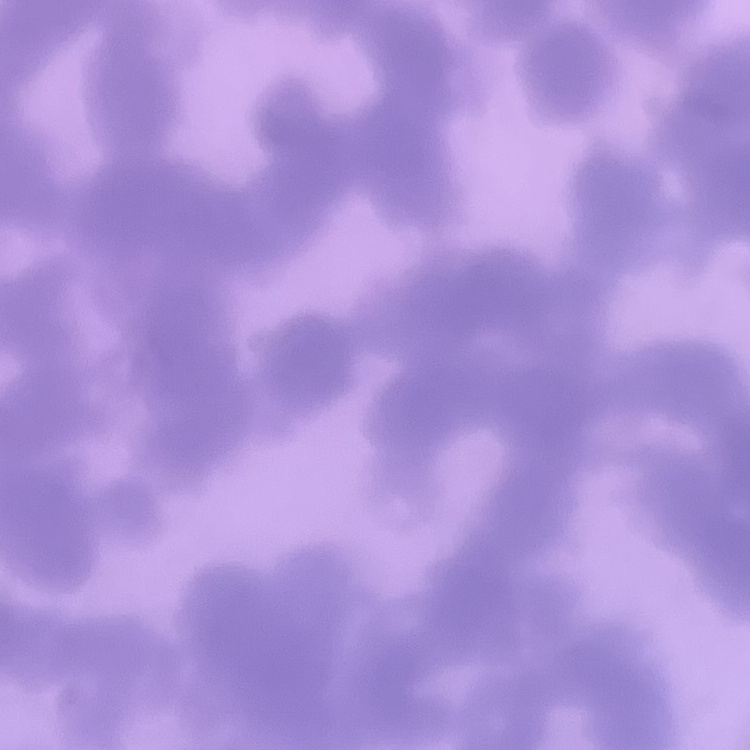 The erythrocytes exhibit rouleaux formation. Stained with either Field's or Giemsa. Square crop of a larger photomicrograph. Thin blood smear.